Outline each blood parasite and name the species.
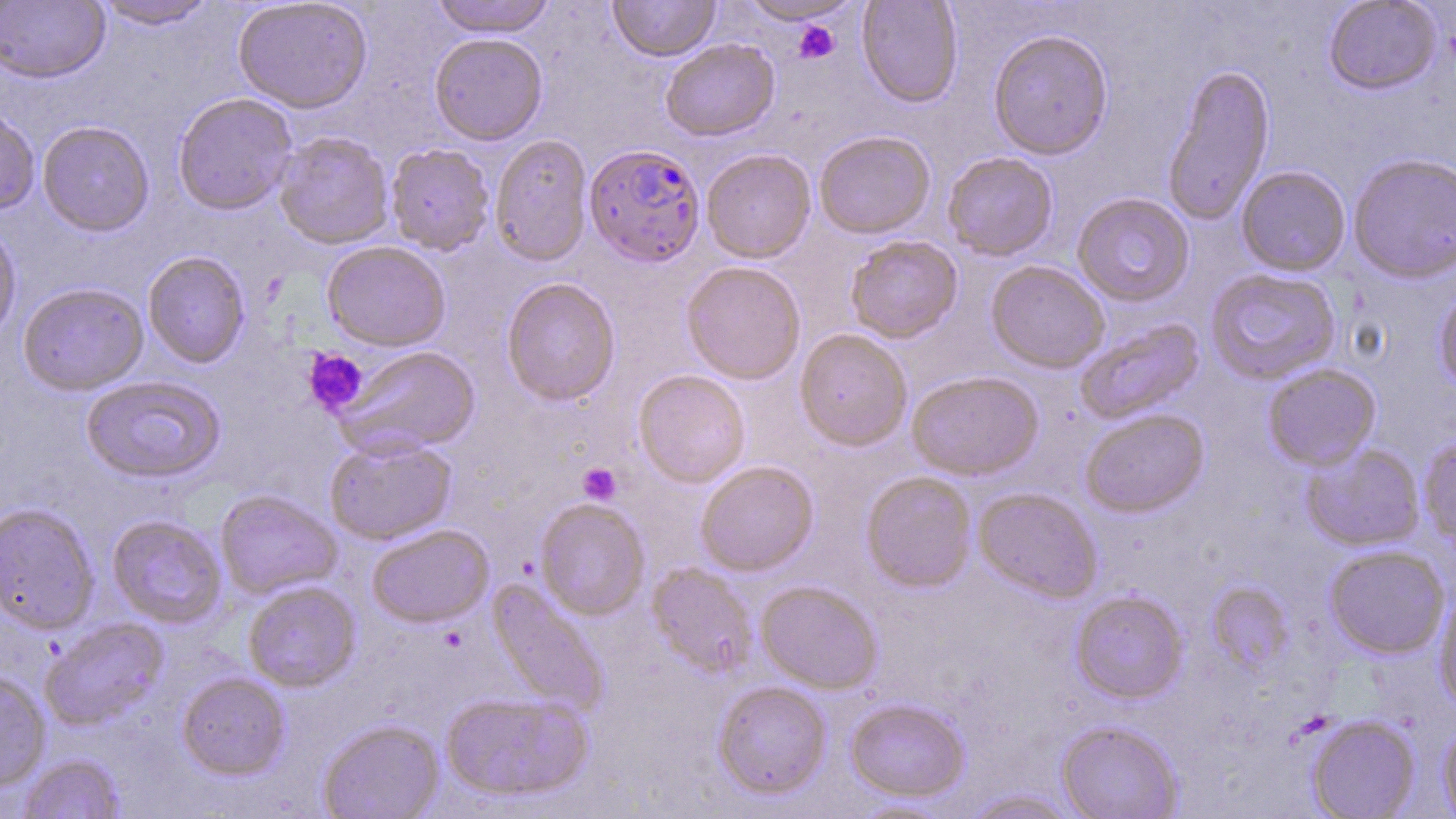

Approximate bounding boxes as (x1, y1, x2, y2) in pixels.
Plasmodium falciparum-infected red blood cells: (584, 145, 706, 268).
No Plasmodium ovale, Plasmodium malariae, Plasmodium vivax, Babesia divergens, or Trypanosoma brucei observed.

Summary:
  - Uninfected red blood cell locations: (92, 0, 218, 30), (232, 0, 373, 114), (429, 0, 557, 38), (608, 0, 720, 62), (857, 0, 963, 108), (1323, 0, 1441, 96), (0, 1, 110, 83), (739, 1, 858, 25), (782, 18, 849, 65), (988, 29, 1113, 160), (429, 33, 547, 145), (661, 38, 779, 141), (1162, 63, 1275, 226), (173, 93, 297, 215), (0, 103, 41, 215), (37, 120, 154, 236), (273, 131, 394, 249), (814, 131, 936, 240), (489, 134, 593, 267), (386, 144, 494, 255), (701, 149, 816, 263), (942, 152, 1058, 261), (1348, 153, 1456, 284), (1236, 166, 1351, 276), (1072, 193, 1195, 307), (0, 219, 21, 345), (846, 235, 963, 343), (322, 241, 450, 351), (142, 251, 250, 368), (681, 261, 806, 385), (986, 261, 1109, 373), (1206, 268, 1341, 385), (500, 277, 621, 407), (18, 283, 149, 395), (1434, 287, 1456, 394), (1074, 318, 1205, 425), (794, 330, 912, 451), (335, 345, 480, 456), (1262, 364, 1381, 471), (633, 370, 751, 488), (906, 372, 1044, 482), (81, 375, 225, 483), (1080, 409, 1209, 517), (324, 436, 456, 545), (1419, 437, 1456, 551), (1301, 444, 1424, 552), (696, 461, 819, 576), (861, 471, 977, 592), (973, 487, 1102, 603), (215, 490, 342, 600), (535, 499, 650, 620), (0, 503, 99, 634), (107, 515, 227, 629), (367, 524, 495, 628), (1324, 545, 1450, 658), (647, 563, 758, 678), (243, 581, 361, 692), (486, 581, 609, 716), (756, 581, 883, 694), (1207, 582, 1294, 675), (1434, 589, 1456, 712), (1070, 591, 1188, 704), (40, 617, 169, 730), (0, 671, 51, 791), (177, 672, 290, 781), (712, 680, 832, 800), (440, 692, 592, 802), (845, 698, 970, 802), (1306, 715, 1420, 819), (317, 719, 445, 819), (1056, 720, 1183, 819), (1439, 721, 1456, 819), (17, 754, 126, 819), (963, 790, 1080, 818), (848, 797, 958, 818)
  - Platelet locations: (793, 21, 841, 63), (304, 349, 369, 415), (578, 463, 621, 505)
  - Slide-level diagnosis: Plasmodium falciparum
  - Field of view: single
  - Magnification: 1000x
  - Image size: 1456×819 pixels
  - Preparation: thin blood smear
  - Stain: May-Grünwald-Giemsa
  - Modality: optical microscopy